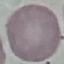

Malaria status: uninfected. Acquired by smartphone through the microscope eyepiece. Cell patch, automatically extracted from a larger field of view and resized to 64 × 64 pixels. Giemsa-stained preparation. Thin smear of blood.